Identify the parasite.
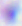

This is Toxoplasma gondii.

{
  "magnification": "400x",
  "modality": "micrograph"
}